Name the blood parasite species.
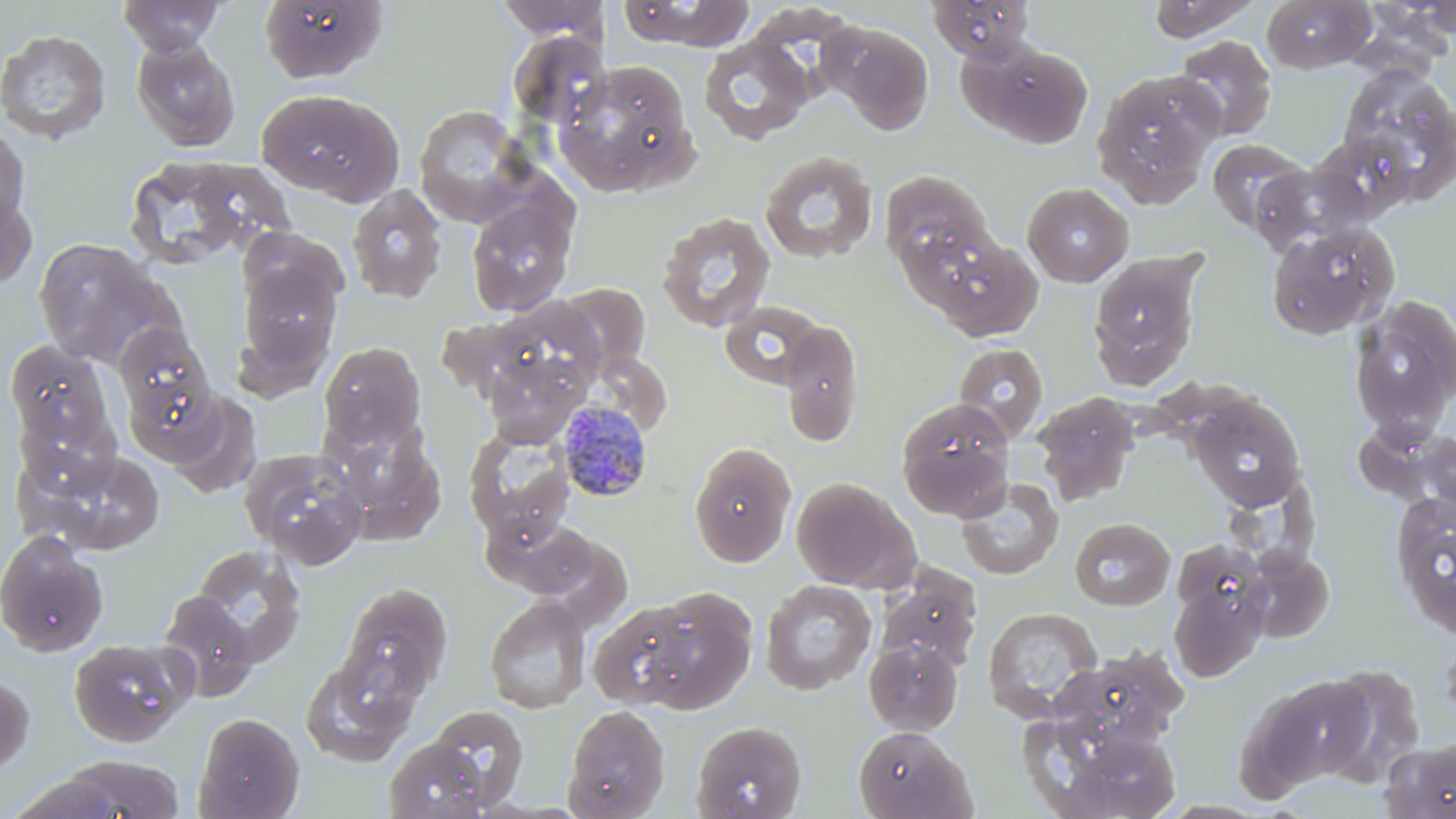
Plasmodium malariae.

Approximate bounding boxes as named x1/y1/x2/y2 corners in pixels. Uninfected red blood cell locations: (x1=118, y1=0, x2=224, y2=55), (x1=259, y1=0, x2=387, y2=85), (x1=618, y1=0, x2=755, y2=50), (x1=928, y1=0, x2=1039, y2=63), (x1=1146, y1=0, x2=1263, y2=42), (x1=1262, y1=0, x2=1376, y2=73), (x1=495, y1=1, x2=609, y2=40), (x1=822, y1=21, x2=933, y2=136), (x1=0, y1=28, x2=111, y2=144), (x1=506, y1=31, x2=610, y2=130), (x1=1174, y1=35, x2=1277, y2=141), (x1=698, y1=37, x2=813, y2=145), (x1=131, y1=38, x2=241, y2=152), (x1=970, y1=42, x2=1094, y2=148), (x1=554, y1=62, x2=696, y2=195), (x1=1335, y1=64, x2=1456, y2=204), (x1=1093, y1=68, x2=1223, y2=207), (x1=256, y1=88, x2=404, y2=204), (x1=413, y1=105, x2=535, y2=228), (x1=0, y1=125, x2=32, y2=235), (x1=1207, y1=139, x2=1309, y2=234), (x1=760, y1=148, x2=879, y2=264), (x1=137, y1=156, x2=245, y2=266), (x1=1249, y1=163, x2=1370, y2=258), (x1=880, y1=170, x2=997, y2=277), (x1=1022, y1=182, x2=1134, y2=286), (x1=0, y1=183, x2=38, y2=294), (x1=347, y1=184, x2=447, y2=302), (x1=466, y1=196, x2=577, y2=316), (x1=656, y1=211, x2=776, y2=333), (x1=1265, y1=220, x2=1400, y2=341), (x1=925, y1=235, x2=1044, y2=342), (x1=33, y1=237, x2=177, y2=369), (x1=1087, y1=250, x2=1204, y2=390), (x1=236, y1=256, x2=343, y2=379), (x1=555, y1=282, x2=652, y2=376), (x1=1348, y1=296, x2=1456, y2=440), (x1=470, y1=297, x2=610, y2=406), (x1=719, y1=300, x2=831, y2=391), (x1=778, y1=319, x2=864, y2=447), (x1=114, y1=322, x2=216, y2=429), (x1=5, y1=340, x2=113, y2=453), (x1=318, y1=341, x2=426, y2=452), (x1=953, y1=342, x2=1049, y2=442), (x1=483, y1=353, x2=584, y2=445), (x1=1185, y1=390, x2=1306, y2=510), (x1=165, y1=391, x2=262, y2=495), (x1=1031, y1=393, x2=1140, y2=507), (x1=895, y1=398, x2=1015, y2=521), (x1=1363, y1=421, x2=1456, y2=515), (x1=330, y1=425, x2=445, y2=544), (x1=463, y1=425, x2=576, y2=548), (x1=688, y1=442, x2=796, y2=567), (x1=22, y1=446, x2=165, y2=556), (x1=240, y1=448, x2=367, y2=568), (x1=1216, y1=463, x2=1327, y2=578), (x1=791, y1=477, x2=917, y2=592), (x1=955, y1=479, x2=1063, y2=580), (x1=1390, y1=490, x2=1456, y2=639), (x1=490, y1=517, x2=606, y2=600), (x1=1070, y1=517, x2=1175, y2=610), (x1=0, y1=531, x2=109, y2=657), (x1=1170, y1=539, x2=1269, y2=634), (x1=1243, y1=542, x2=1350, y2=641), (x1=189, y1=545, x2=306, y2=666), (x1=1169, y1=575, x2=1269, y2=682), (x1=760, y1=579, x2=877, y2=695), (x1=874, y1=579, x2=981, y2=675), (x1=339, y1=582, x2=453, y2=702), (x1=631, y1=587, x2=757, y2=713), (x1=156, y1=592, x2=259, y2=702), (x1=485, y1=595, x2=591, y2=714), (x1=588, y1=601, x2=701, y2=708), (x1=983, y1=606, x2=1103, y2=722), (x1=1438, y1=621, x2=1456, y2=733), (x1=69, y1=638, x2=196, y2=748), (x1=864, y1=638, x2=963, y2=735), (x1=1048, y1=651, x2=1187, y2=755), (x1=301, y1=652, x2=420, y2=766), (x1=1319, y1=663, x2=1427, y2=785), (x1=0, y1=672, x2=35, y2=778), (x1=1245, y1=675, x2=1376, y2=793), (x1=424, y1=705, x2=529, y2=809), (x1=563, y1=705, x2=670, y2=819), (x1=194, y1=712, x2=304, y2=818), (x1=691, y1=720, x2=807, y2=819), (x1=1035, y1=725, x2=1185, y2=818), (x1=854, y1=726, x2=974, y2=818), (x1=382, y1=737, x2=499, y2=819), (x1=1381, y1=738, x2=1456, y2=818), (x1=59, y1=753, x2=186, y2=818), (x1=10, y1=775, x2=124, y2=818), (x1=1155, y1=800, x2=1273, y2=818). Plasmodium malariae-infected red blood cell locations: (x1=557, y1=400, x2=656, y2=503). Thin blood film. One field of a larger specimen. Optical microscopy. May-Grünwald-Giemsa-stained preparation. Captured at 1000x magnification. Image is 1456×819 pixels.